Outline each blood parasite and name the species.
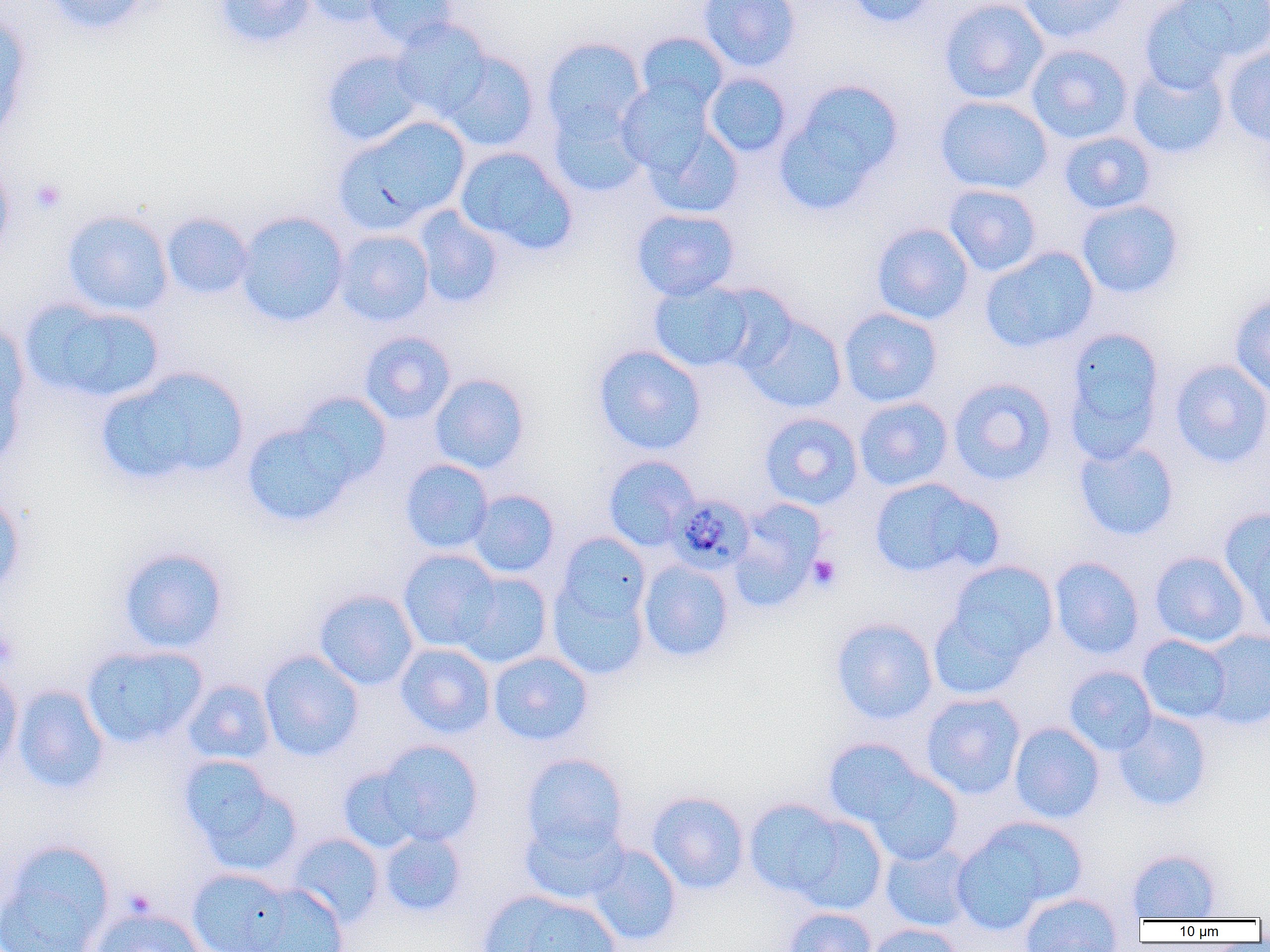

Approximate bounding boxes as (x1, y1, x2, y2) in pixels.
Plasmodium malariae-infected red blood cells: (667, 493, 755, 575).
No Plasmodium falciparum, Plasmodium ovale, Plasmodium vivax, Babesia divergens, or Trypanosoma brucei observed.

Summary:
  - Platelet locations: (30, 178, 66, 215), (807, 554, 842, 591), (0, 625, 19, 671)
  - Uninfected red blood cell locations: (44, 0, 155, 35), (214, 0, 316, 49), (301, 0, 397, 28), (363, 0, 458, 49), (698, 0, 800, 72), (846, 0, 938, 28), (939, 0, 1049, 105), (1019, 0, 1131, 44), (1139, 0, 1250, 91), (0, 16, 33, 143), (390, 19, 493, 120), (636, 32, 729, 112), (541, 38, 646, 138), (1025, 44, 1134, 144), (1221, 47, 1270, 145), (320, 49, 426, 147), (439, 50, 540, 151), (1127, 60, 1229, 159), (703, 72, 792, 157), (776, 79, 904, 212), (615, 80, 714, 174), (935, 95, 1054, 195), (548, 101, 648, 197), (334, 116, 471, 234), (643, 122, 744, 219), (1058, 131, 1157, 215), (455, 146, 577, 256), (0, 155, 15, 260), (944, 184, 1042, 276), (1075, 199, 1185, 299), (413, 207, 505, 309), (630, 208, 740, 301), (62, 210, 173, 317), (161, 212, 254, 299), (236, 212, 349, 328), (871, 222, 975, 325), (333, 229, 434, 326), (980, 247, 1099, 353), (647, 278, 762, 374), (1230, 292, 1270, 399), (21, 299, 166, 404), (838, 307, 943, 407), (738, 312, 848, 414), (0, 319, 31, 468), (1063, 326, 1166, 460), (360, 331, 456, 424), (593, 344, 707, 455), (1168, 359, 1270, 469), (96, 366, 250, 488), (429, 373, 530, 473), (947, 377, 1057, 485), (294, 392, 392, 486), (853, 396, 954, 491), (758, 412, 863, 510), (241, 422, 357, 528), (1074, 439, 1179, 541), (602, 455, 700, 551), (400, 459, 494, 555), (869, 477, 1001, 580), (468, 489, 560, 578), (0, 493, 26, 598), (729, 499, 827, 611), (1219, 509, 1270, 631), (555, 532, 651, 627), (116, 546, 229, 653), (398, 549, 501, 652), (1149, 551, 1250, 648), (1049, 557, 1144, 659), (637, 559, 734, 662), (946, 561, 1059, 663), (455, 571, 553, 669), (548, 580, 650, 680), (313, 589, 419, 691), (927, 607, 1028, 701), (830, 617, 938, 725), (1200, 629, 1270, 730), (1137, 634, 1232, 724), (395, 643, 495, 739), (81, 644, 208, 748), (259, 650, 364, 761), (488, 651, 593, 746), (1064, 665, 1157, 756), (0, 667, 23, 773), (182, 679, 276, 765), (13, 685, 111, 794), (920, 693, 1025, 799), (1112, 710, 1212, 812), (1009, 722, 1105, 823), (823, 738, 926, 829), (376, 740, 483, 846), (521, 753, 628, 855), (177, 755, 301, 875), (338, 766, 425, 853), (865, 769, 963, 866), (647, 791, 749, 894), (743, 798, 848, 898), (520, 815, 629, 905), (791, 815, 888, 915), (952, 817, 1083, 930), (379, 830, 467, 917), (287, 833, 385, 928), (0, 840, 115, 952), (880, 842, 976, 932), (586, 844, 682, 947), (1126, 848, 1222, 921), (187, 867, 293, 952), (246, 883, 349, 952), (478, 890, 621, 952), (1020, 892, 1123, 951), (89, 906, 208, 952), (784, 908, 877, 952), (865, 923, 964, 952)
  - Slide-level diagnosis: Plasmodium malariae
  - Image size: 1270×952 pixels
  - Field of view: one of a larger specimen
  - Modality: light microscopy
  - Preparation: thin blood smear
  - Magnification: 1000x